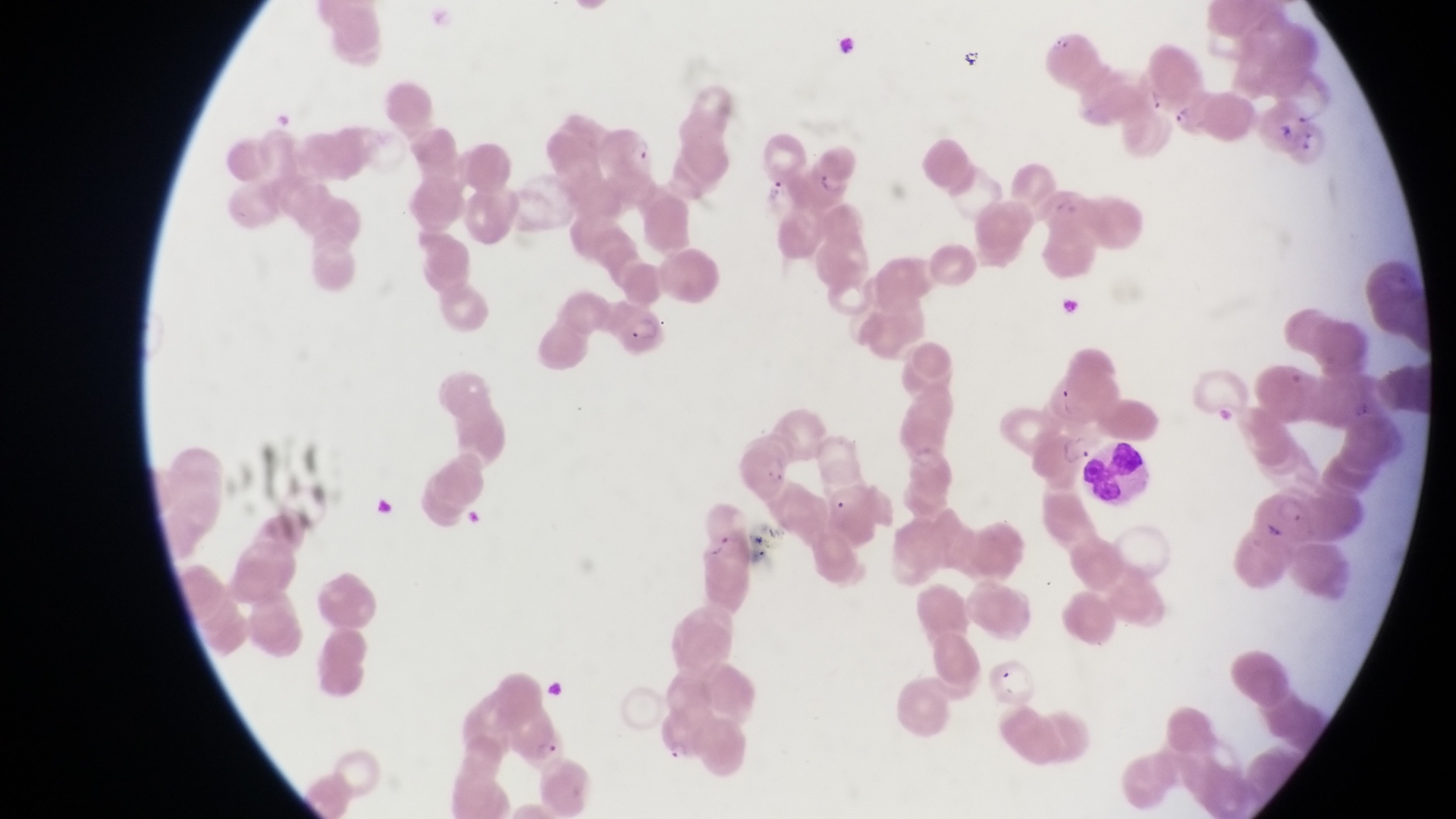 Approximate bounding boxes as (left, top, right, bottom) in pixels. Parasitised red blood cell locations: (594, 124, 657, 180), (808, 148, 864, 197), (614, 310, 667, 360), (732, 431, 793, 498), (512, 716, 567, 774), (655, 717, 716, 763). Leukocyte locations: (1080, 446, 1160, 505). Artifact (platelet-like body, stain precipitate, or debris) locations: (954, 42, 987, 78). Captured by a smartphone held over the eyepiece of an Olympus CX-23 microscope. Collected in Uganda. At a magnification of 1000x. Image is 1456×819 pixels. Single field of view. Thin blood smear.